Locate and identify every blood parasite.
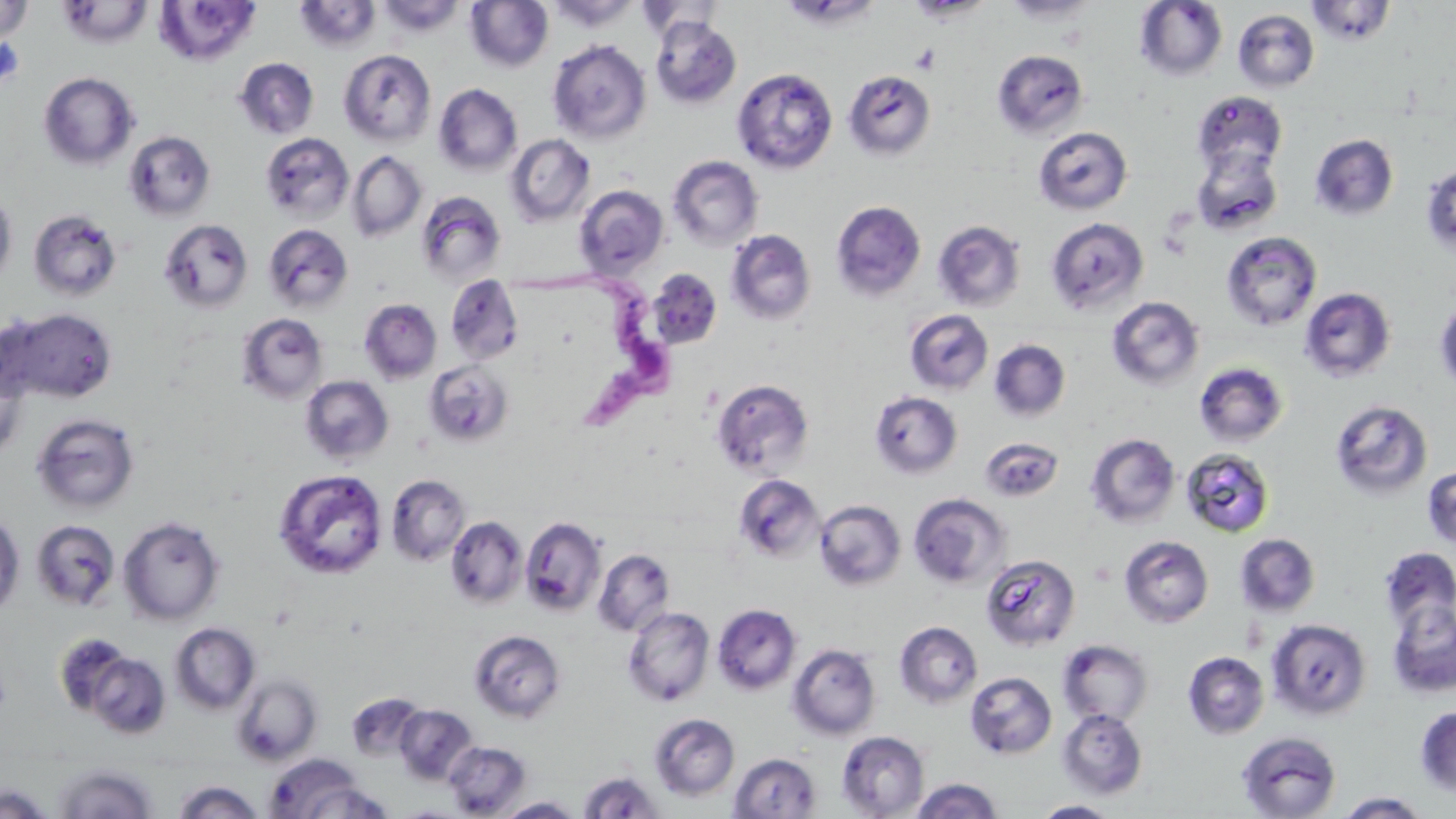

Approximate bounding boxes as [x1, y1, x2, y2] in pixels.
Trypanosoma brucei: [515, 267, 688, 430].
No Plasmodium falciparum, Plasmodium ovale, Plasmodium malariae, Plasmodium vivax, or Babesia divergens observed.

Platelet locations: [911, 45, 940, 73]. Uninfected red blood cell locations: [376, 0, 465, 37], [547, 0, 639, 31], [636, 0, 726, 42], [906, 0, 992, 22], [1002, 0, 1098, 25], [0, 1, 33, 42], [57, 1, 153, 48], [153, 1, 262, 67], [293, 1, 381, 52], [465, 1, 554, 72], [1135, 1, 1228, 81], [1306, 1, 1396, 47], [1233, 9, 1320, 92], [650, 16, 742, 109], [547, 39, 652, 144], [338, 49, 436, 146], [992, 49, 1088, 138], [234, 57, 319, 140], [732, 67, 838, 174], [844, 70, 936, 161], [38, 72, 139, 170], [434, 84, 522, 176], [1192, 91, 1287, 176], [1033, 126, 1132, 215], [123, 131, 216, 221], [260, 133, 355, 224], [505, 134, 595, 226], [1310, 134, 1399, 220], [1190, 146, 1283, 237], [347, 151, 426, 243], [668, 155, 764, 251], [1421, 164, 1456, 257], [575, 185, 669, 279], [0, 190, 16, 288], [415, 190, 507, 285], [830, 200, 926, 301], [28, 209, 122, 302], [1045, 216, 1149, 316], [159, 218, 254, 313], [933, 220, 1025, 313], [262, 223, 354, 314], [725, 229, 816, 325], [1221, 231, 1322, 331], [647, 269, 722, 350], [445, 275, 524, 365], [1299, 287, 1395, 382], [1106, 296, 1205, 392], [1435, 297, 1456, 394], [359, 299, 441, 383], [3, 306, 117, 404], [904, 310, 993, 395], [237, 313, 328, 404], [989, 339, 1070, 422], [423, 360, 513, 447], [1194, 362, 1289, 447], [299, 375, 394, 464], [712, 379, 814, 477], [870, 390, 962, 479], [1329, 399, 1433, 501], [31, 413, 140, 514], [1085, 433, 1180, 528], [980, 436, 1063, 503], [1181, 447, 1275, 537], [1422, 464, 1456, 552], [274, 468, 388, 580], [387, 474, 470, 566], [734, 474, 824, 564], [908, 492, 1011, 590], [814, 499, 906, 592], [0, 512, 24, 616], [118, 515, 224, 625], [446, 516, 527, 608], [520, 517, 606, 617], [31, 519, 121, 610], [1235, 533, 1321, 618], [1119, 535, 1214, 628], [1380, 547, 1456, 633], [593, 548, 676, 636], [980, 553, 1081, 651], [1387, 600, 1456, 698], [712, 603, 802, 695], [623, 606, 714, 707], [1266, 617, 1372, 720], [894, 621, 982, 708], [169, 623, 260, 715], [468, 629, 566, 723], [1058, 639, 1154, 728], [787, 643, 881, 741], [84, 651, 171, 739], [1183, 651, 1270, 740], [965, 671, 1057, 760], [231, 674, 321, 766], [346, 692, 426, 761], [395, 705, 477, 785], [1414, 706, 1456, 797], [1057, 708, 1148, 800], [649, 713, 740, 801], [836, 730, 929, 818], [1236, 731, 1342, 818], [443, 740, 530, 817], [729, 752, 821, 818], [264, 754, 375, 819], [52, 763, 159, 818], [579, 770, 664, 818], [909, 777, 1003, 819], [172, 780, 265, 819], [0, 784, 56, 818], [1334, 791, 1432, 818], [496, 796, 584, 818], [1032, 800, 1120, 817]. Slide-level diagnosis: Trypanosoma brucei. Light microscopy. May-Grünwald-Giemsa-stained preparation. 1000x magnification. One field of a larger specimen. Image is 1456×819 pixels. Thin blood smear.